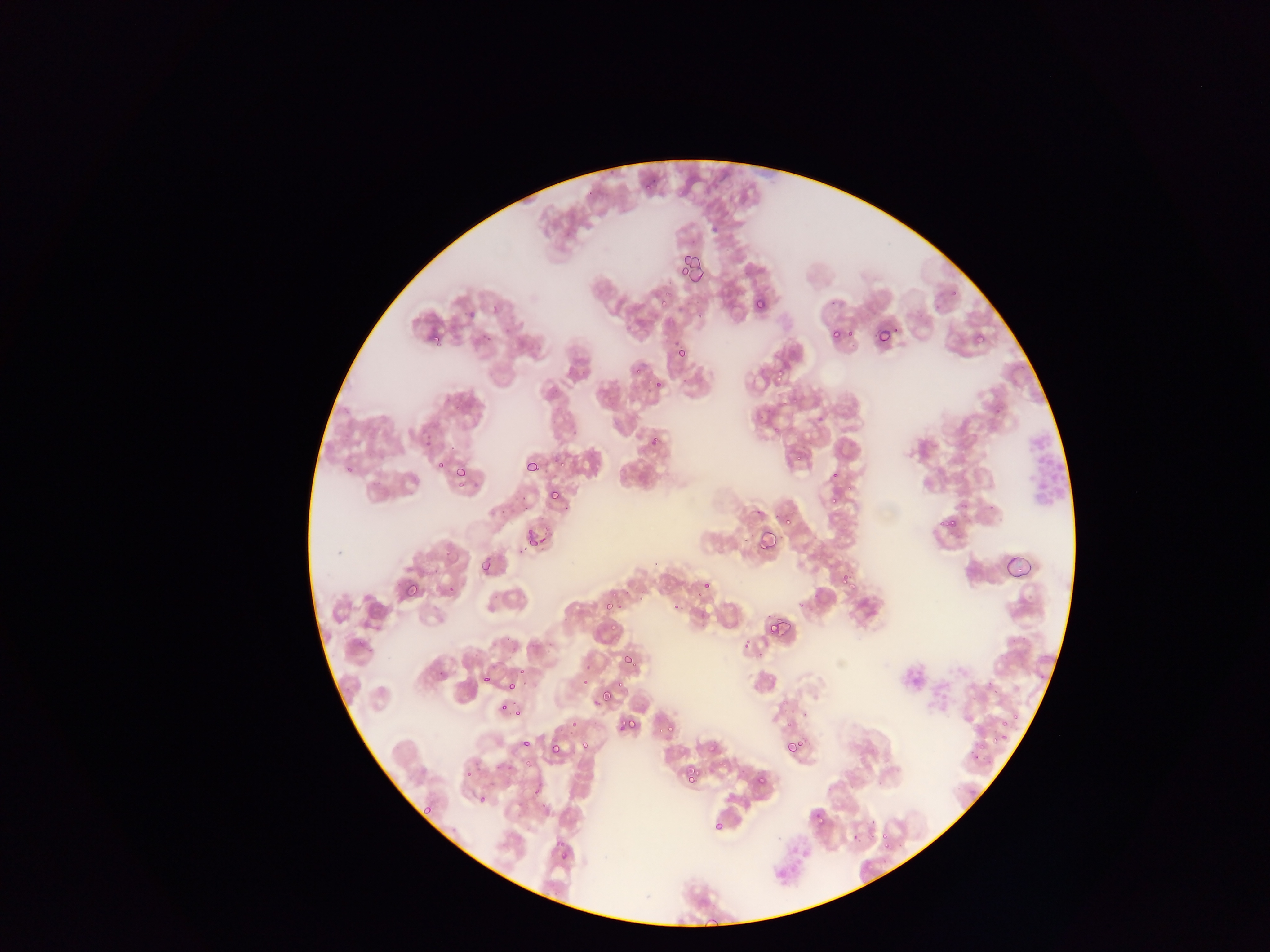

{
  "capture": "mobile-phone photograph through a microscope",
  "field_of_view": "single",
  "malaria_parasite_locations": "approximate bounding boxes as left top right bottom in pixels: 645 181 653 190; 677 253 692 270; 677 253 700 278; 659 293 670 311; 754 299 765 310; 873 327 889 343; 829 328 841 340; 428 332 439 342; 974 334 985 344; 676 348 687 360; 776 366 789 378; 652 378 662 388; 554 456 566 466; 524 459 540 473; 435 462 446 470; 453 465 466 478; 830 489 844 503; 549 490 560 500; 779 512 792 525; 940 515 957 530; 758 529 777 550; 534 536 548 547; 481 561 491 572; 840 572 852 585; 400 579 419 598; 701 582 710 590; 444 584 455 595; 602 602 616 612; 672 604 681 613; 773 617 791 636; 766 618 784 637; 610 623 619 634; 620 654 637 664; 584 664 595 670; 482 674 491 682; 582 676 595 686; 616 678 623 688; 506 680 517 691; 598 691 613 704; 499 704 508 713; 513 706 524 715; 617 717 635 732; 569 720 580 727; 996 721 1014 728; 663 723 675 735; 521 739 531 748; 988 739 997 745; 579 741 588 751; 704 741 717 754; 784 741 800 755; 550 745 561 755; 524 758 534 767; 506 765 516 770; 684 768 698 783; 462 773 474 779; 754 775 765 786; 532 789 542 796; 477 793 486 803; 424 804 432 813; 813 810 824 820; 713 819 725 832; 880 832 890 845; 557 854 567 861",
  "country": "Ghana",
  "preparation": "thin blood film",
  "image_size": "1270×952 pixels"
}